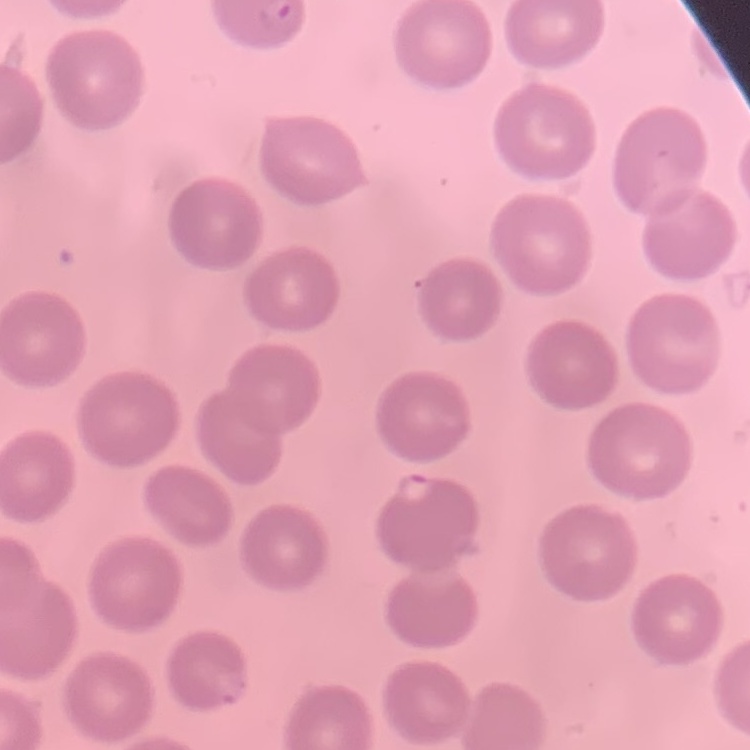
Summary:
  - Red blood cell morphology: no rouleaux formation
  - Stain: Field's or Giemsa
  - Image type: square crop of a larger photomicrograph
  - Preparation: thin peripheral smear